State which parasite is depicted.
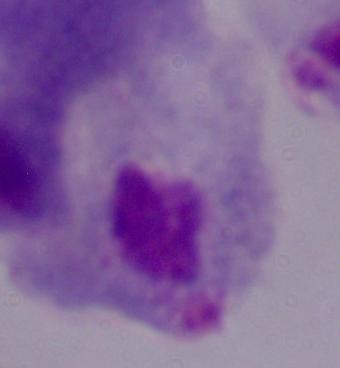

A trichomonad.

1000x magnification. Photomicrograph.